Describe the morphology of the red blood cells.
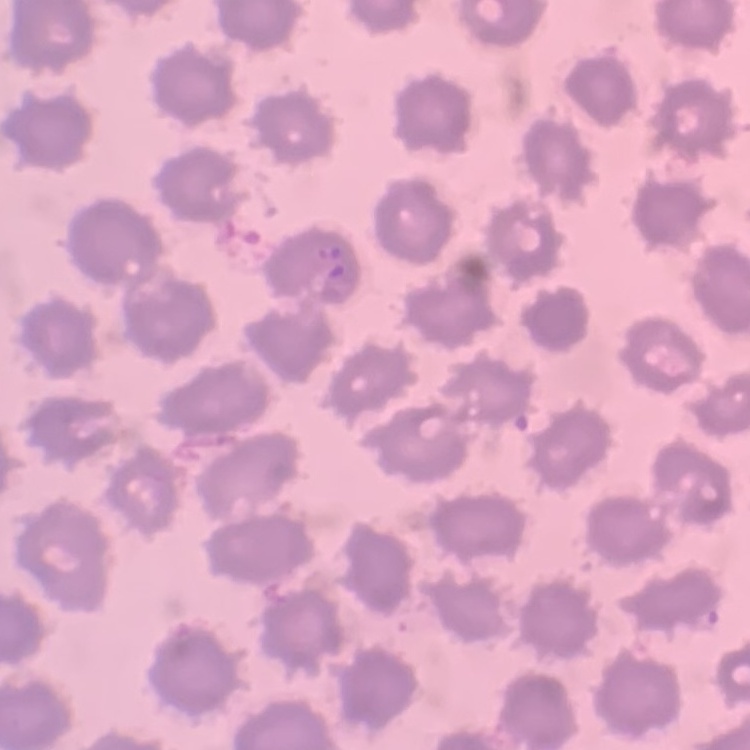
They show no rouleaux formation.

Thin blood smear. Square crop of a larger photomicrograph. Field's or Giemsa stain.